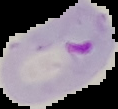

Summary:
  - Image type: segmented cell region with the area outside set to black
  - Result: malaria parasites identified
  - Preparation: thin blood smear
  - Image size: 118×109 pixels